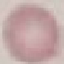
Summary:
  - Malaria status: uninfected
  - Preparation: thin blood smear
  - Capture: smartphone camera at the microscope eyepiece
  - Image type: automatically extracted cell patch, resized to 64 × 64 pixels
  - Stain: Giemsa